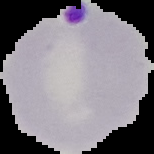

image size = 154×154 pixels
preparation = thin blood film
result = malaria parasites detected
image type = segmented cell region on a black background